Locate every blood parasite and identify its species.
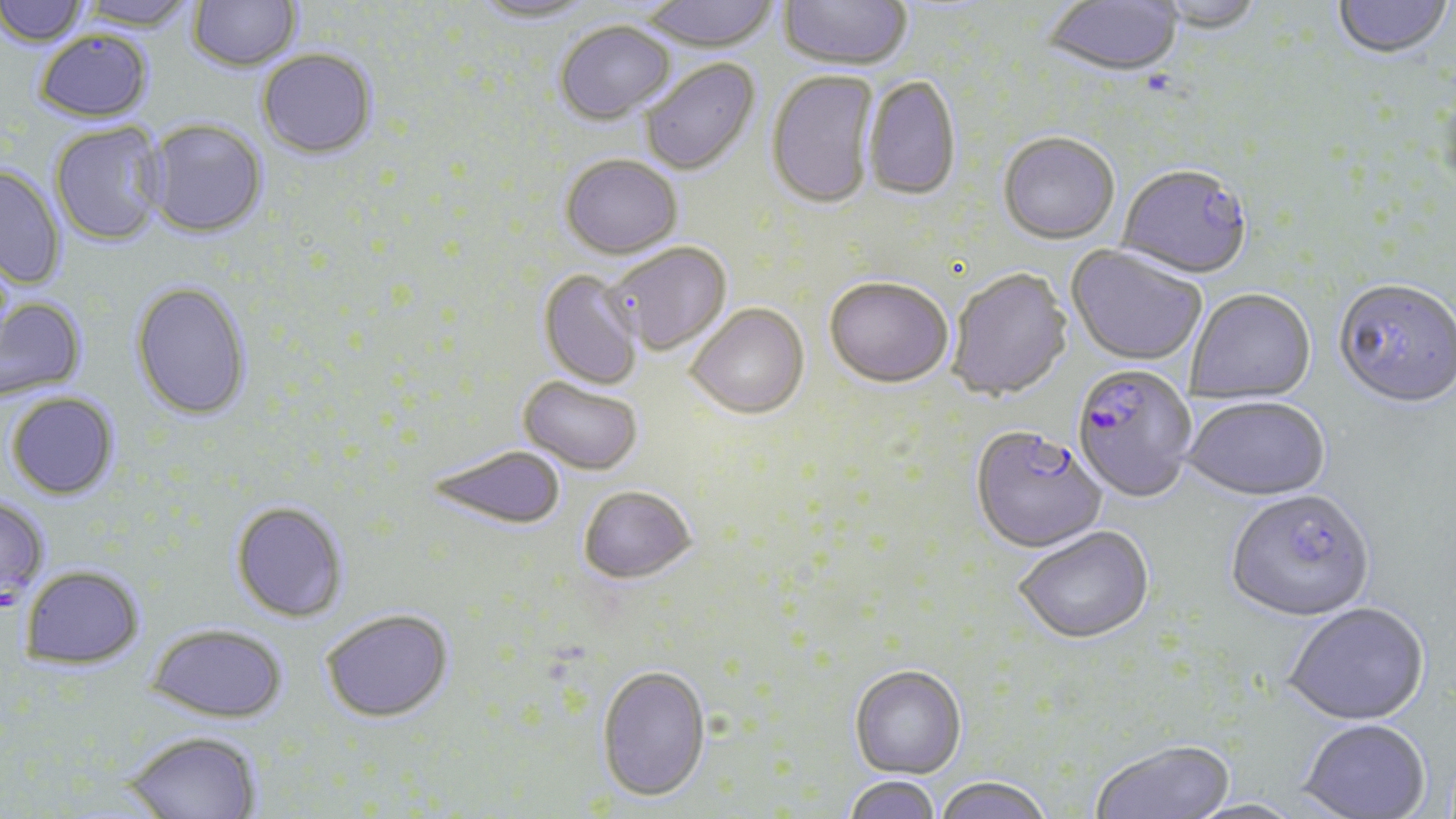
Approximate bounding boxes as (x1, y1, x2, y2) in pixels.
Plasmodium falciparum-infected red blood cells: (1118, 167, 1253, 282), (1071, 367, 1196, 504), (971, 429, 1106, 556).
No Plasmodium ovale, Plasmodium malariae, Plasmodium vivax, Babesia divergens, or Trypanosoma brucei observed.

Summary:
  - Uninfected red blood cell locations: (0, 0, 90, 49), (76, 0, 197, 33), (188, 0, 301, 72), (470, 0, 600, 26), (639, 0, 781, 54), (1043, 0, 1183, 81), (1332, 0, 1453, 61), (778, 1, 912, 73), (1152, 1, 1266, 36), (555, 23, 676, 127), (34, 31, 153, 125), (257, 50, 378, 162), (640, 59, 761, 178), (767, 71, 880, 211), (863, 76, 961, 203), (144, 120, 267, 240), (50, 124, 166, 247), (998, 135, 1120, 247), (560, 157, 683, 262), (0, 165, 65, 289), (608, 243, 732, 357), (1065, 247, 1205, 368), (538, 270, 644, 391), (948, 271, 1073, 403), (824, 280, 952, 392), (1334, 282, 1456, 412), (130, 283, 252, 423), (1186, 291, 1316, 405), (0, 297, 88, 405), (685, 305, 810, 421), (517, 377, 643, 476), (6, 394, 119, 502), (1184, 399, 1330, 504), (426, 446, 566, 532), (579, 487, 697, 585), (1225, 493, 1375, 626), (0, 499, 50, 611), (230, 502, 349, 624), (1014, 528, 1155, 647), (20, 568, 146, 674), (1285, 605, 1430, 728), (320, 611, 454, 725), (146, 626, 287, 726), (849, 667, 967, 781), (596, 668, 711, 804), (1297, 722, 1430, 819), (123, 732, 262, 819), (1090, 742, 1234, 819), (842, 776, 941, 819), (933, 779, 1054, 819), (1183, 799, 1309, 819)
  - Slide-level diagnosis: Plasmodium falciparum
  - Magnification: 1000x
  - Stain: May-Grünwald-Giemsa
  - Preparation: thin blood film
  - Modality: optical microscopy
  - Image size: 1456×819 pixels
  - Field of view: single